Outline every Plasmodium parasite, every leukocyte, and every artifact (stain precipitate or debris).
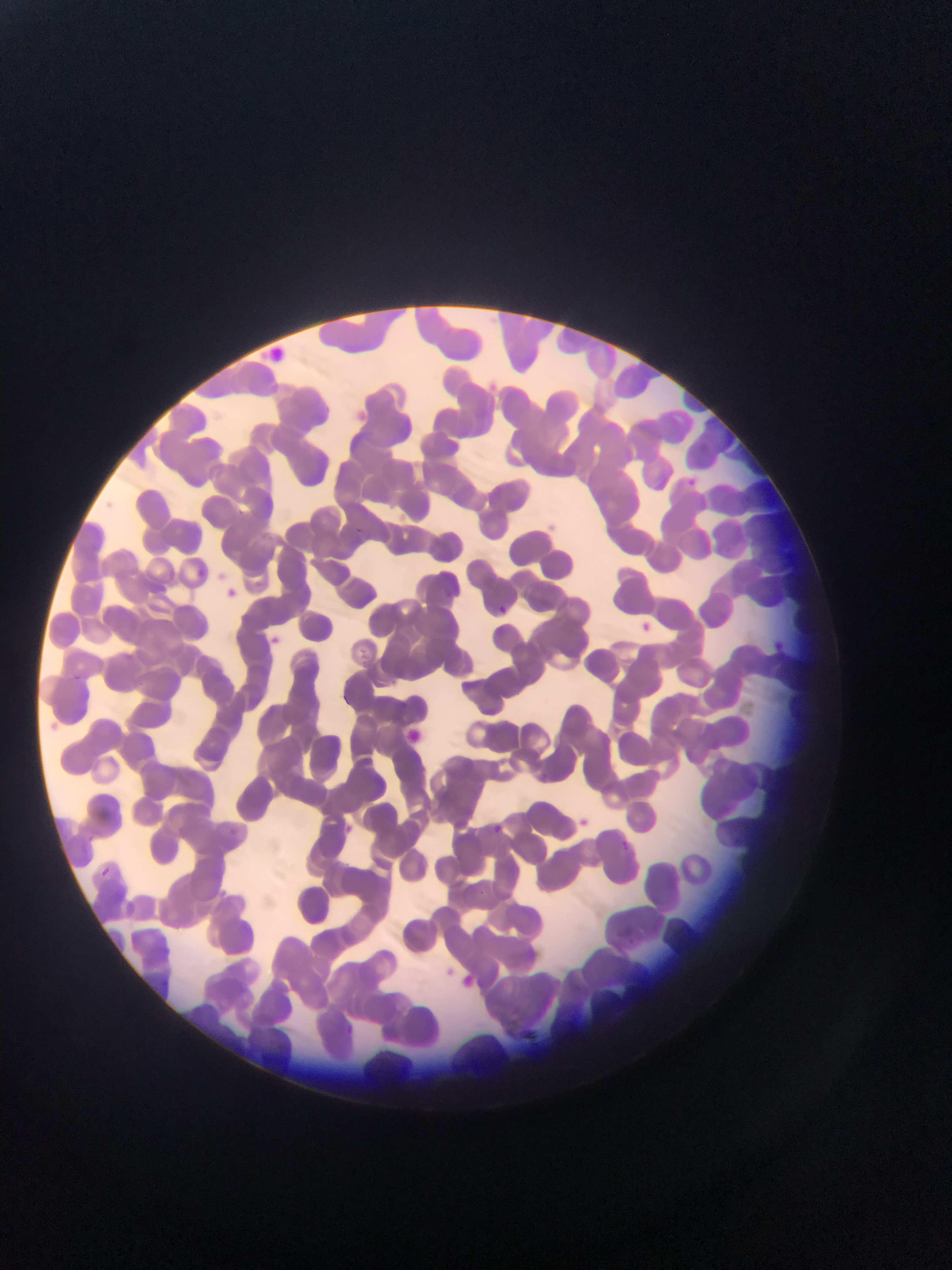

Approximate bounding boxes as (left, top, right, bottom) in pixels.
No Plasmodium parasites observed.
Leukocytes: (224, 582, 239, 599), (493, 601, 511, 617), (643, 617, 668, 644), (271, 627, 286, 645), (579, 810, 594, 831), (491, 818, 514, 839), (627, 929, 641, 947).

capture = mobile-phone photograph through a microscope
field of view = single
image size = 952×1270 pixels
country = Ghana
preparation = thin blood smear